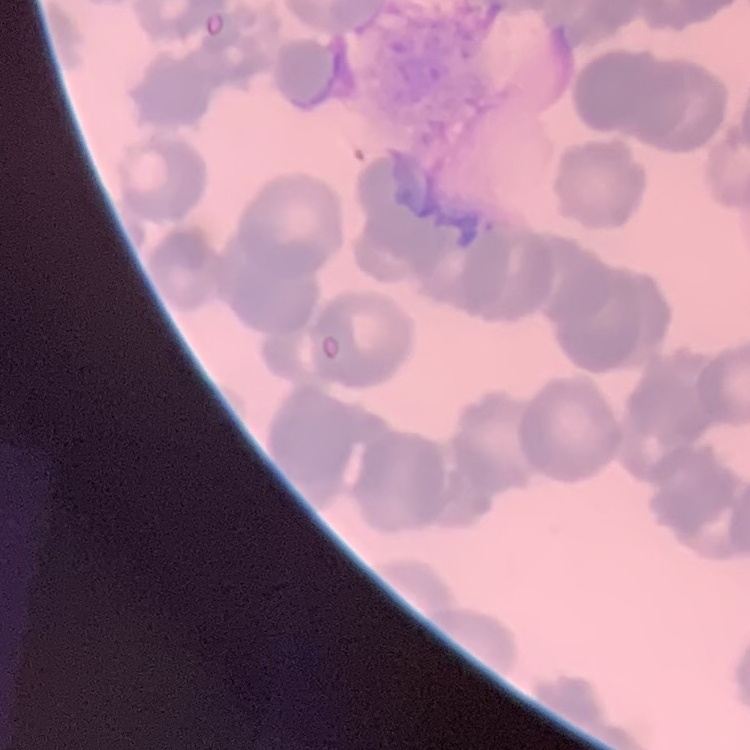

Summary:
  - Red blood cell morphology: rouleaux formation
  - Image type: one tile cut from a larger photomicrograph
  - Stain: Field's or Giemsa
  - Preparation: thin blood film